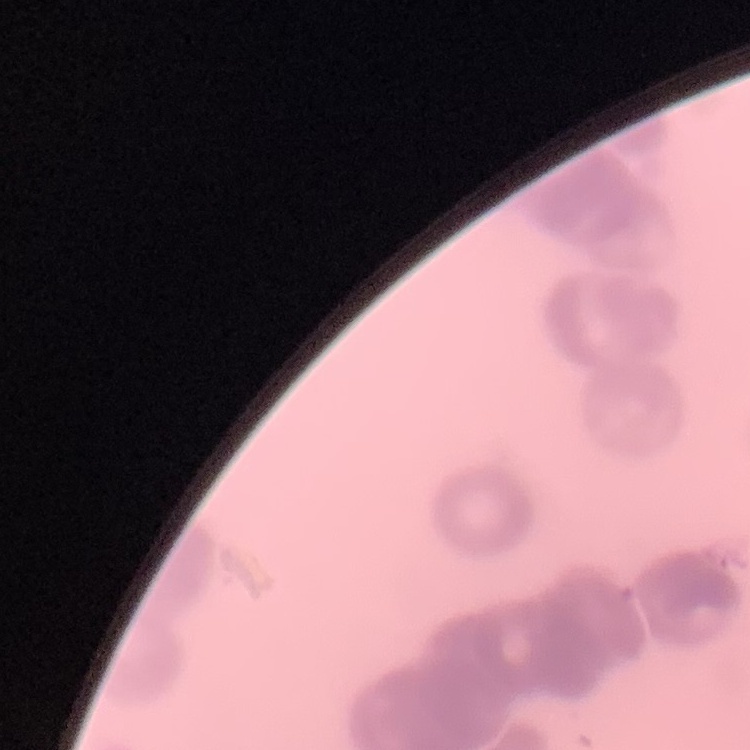

The red blood cells show rouleaux formation. Thin blood film. One tile cut from a larger photomicrograph. Stained with either Field's or Giemsa.